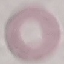
Malaria status: uninfected. Cell patch, automatically extracted from a larger field of view and resized to 64 × 64 pixels. Photographed with a smartphone camera at the microscope eyepiece. Thin blood smear. Giemsa-stained preparation.